Name the parasite shown.
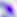

Toxoplasma gondii.

Captured at 400x magnification. Micrograph.